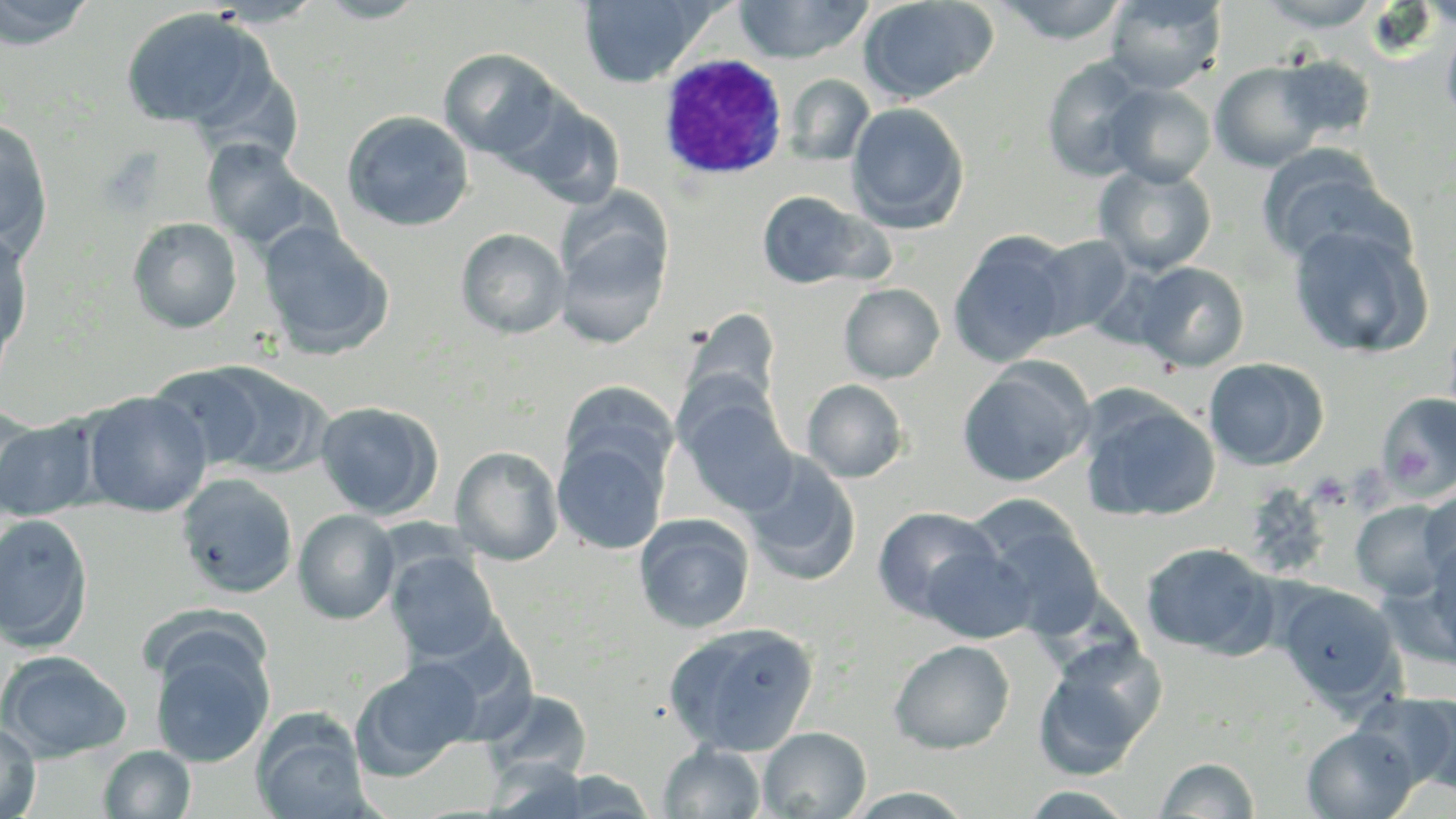 Approximate bounding boxes as (x1, y1, x2, y2) in pixels. Uninfected red blood cell locations: (0, 0, 96, 48), (314, 0, 428, 23), (735, 0, 873, 64), (858, 0, 998, 103), (995, 0, 1130, 45), (1104, 0, 1226, 93), (1256, 0, 1386, 30), (579, 1, 712, 87), (119, 7, 275, 135), (1441, 17, 1456, 132), (439, 48, 564, 161), (1040, 55, 1153, 181), (1273, 55, 1377, 144), (1210, 61, 1331, 172), (784, 74, 874, 165), (1104, 83, 1216, 187), (509, 96, 626, 209), (846, 102, 969, 233), (342, 110, 474, 232), (0, 118, 53, 257), (201, 138, 320, 251), (1256, 145, 1401, 269), (1094, 162, 1217, 276), (756, 190, 878, 291), (554, 208, 672, 350), (128, 217, 242, 334), (257, 220, 395, 359), (1288, 221, 1433, 359), (0, 226, 34, 369), (456, 227, 570, 339), (948, 230, 1074, 367), (1027, 233, 1136, 340), (1131, 261, 1250, 372), (839, 283, 945, 383), (683, 306, 782, 413), (1203, 357, 1329, 471), (168, 360, 328, 479), (957, 360, 1093, 487), (802, 379, 908, 482), (559, 382, 678, 489), (676, 388, 798, 516), (80, 391, 213, 517), (1078, 391, 1221, 524), (1375, 393, 1456, 499), (313, 401, 444, 519), (1, 405, 43, 513), (0, 416, 100, 522), (552, 438, 668, 555), (450, 445, 564, 565), (739, 450, 861, 585), (175, 472, 298, 599), (1418, 486, 1456, 586), (965, 498, 1108, 642), (1350, 500, 1454, 601), (872, 505, 999, 619), (293, 509, 400, 624), (634, 513, 755, 633), (0, 514, 94, 650), (1424, 536, 1456, 664), (1139, 542, 1278, 658), (923, 545, 1035, 644), (387, 551, 501, 664), (1275, 583, 1404, 710), (663, 621, 820, 755), (1032, 636, 1167, 779), (889, 639, 1015, 754), (150, 642, 273, 767), (0, 650, 132, 762), (352, 658, 480, 779), (481, 688, 593, 785), (1367, 691, 1456, 793), (252, 711, 373, 819), (0, 721, 40, 818), (758, 726, 871, 818), (1302, 726, 1419, 818), (658, 743, 765, 819), (98, 745, 196, 818), (1156, 756, 1260, 817), (548, 769, 658, 817), (1017, 787, 1139, 818). White blood cell locations: (657, 53, 788, 180). Slide-level diagnosis: Plasmodium ovale. 1000x magnification. Image is 1456×819 pixels. Single field of view. May-Grünwald-Giemsa-stained preparation. Light microscopy. Thin blood film.